Name the blood parasite species.
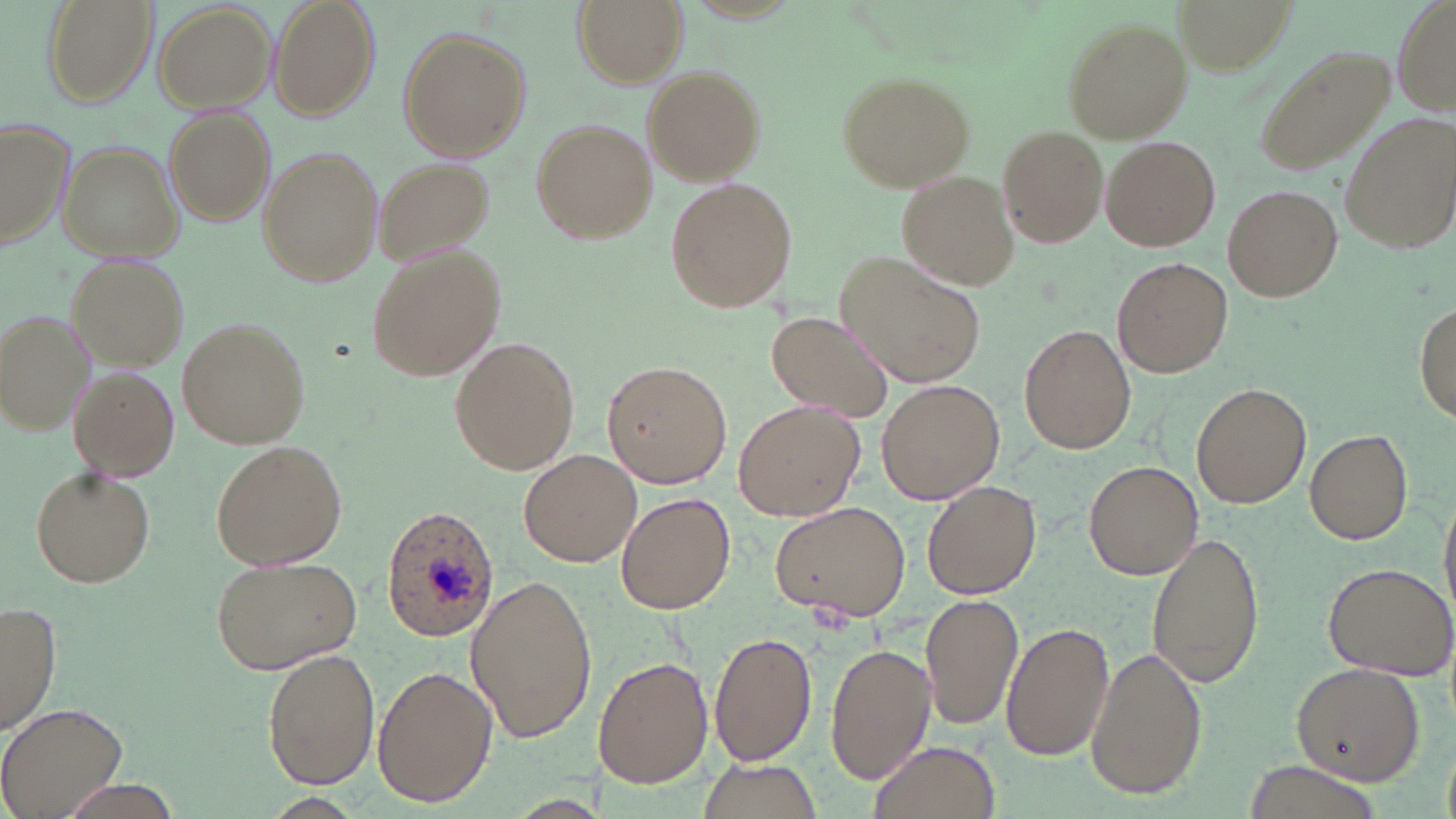
Plasmodium ovale.

modality = optical microscopy
Plasmodium ovale-infected red blood cell locations = approximate bounding boxes as (x1, y1, x2, y2) in pixels: (381, 507, 500, 642)
image size = 1456×819 pixels
magnification = 1000x
preparation = thin blood smear
uninfected red blood cell locations = approximate bounding boxes as (x1, y1, x2, y2) in pixels: (41, 0, 158, 107), (270, 0, 380, 120), (571, 0, 688, 88), (1174, 0, 1298, 77), (1392, 0, 1455, 120), (153, 2, 278, 112), (1063, 18, 1191, 143), (398, 27, 530, 162), (1251, 44, 1393, 177), (642, 68, 765, 184), (836, 71, 975, 191), (164, 109, 276, 224), (1341, 114, 1455, 255), (530, 118, 659, 245), (0, 119, 74, 254), (997, 126, 1108, 248), (1102, 136, 1219, 251), (59, 141, 181, 263), (257, 145, 384, 289), (373, 157, 496, 264), (896, 170, 1020, 291), (664, 177, 799, 313), (1223, 185, 1341, 300), (365, 247, 506, 381), (837, 251, 988, 392), (67, 256, 186, 368), (1114, 257, 1233, 378), (1415, 303, 1454, 419), (1, 308, 96, 435), (766, 310, 889, 422), (179, 317, 311, 449), (1020, 324, 1136, 454), (449, 337, 580, 475), (600, 359, 731, 490), (71, 370, 179, 479), (877, 379, 1003, 504), (1192, 384, 1311, 508), (732, 399, 865, 521), (1304, 430, 1412, 545), (210, 440, 348, 572), (519, 449, 642, 568), (1085, 461, 1202, 580), (30, 465, 157, 589), (923, 480, 1040, 599), (1439, 489, 1456, 626), (616, 492, 736, 615), (772, 499, 913, 622), (1146, 531, 1265, 689), (210, 555, 363, 676), (1322, 561, 1455, 679), (466, 574, 599, 745), (920, 594, 1024, 729), (1, 602, 61, 735), (1001, 621, 1114, 763), (708, 633, 821, 770), (825, 642, 936, 782), (1086, 645, 1207, 802), (262, 647, 380, 790), (593, 656, 712, 789), (1289, 663, 1425, 785), (371, 666, 496, 808), (1, 702, 129, 819), (868, 738, 1002, 819), (693, 758, 824, 818), (1234, 760, 1384, 819), (52, 778, 183, 819)
stain = May-Grünwald-Giemsa
field of view = single